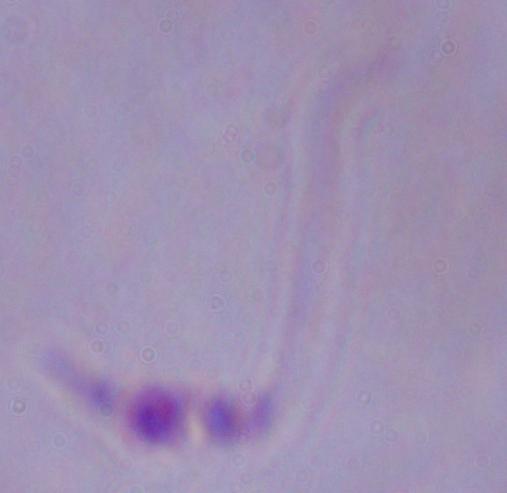
Summary:
  - Identification: Leishmania
  - Modality: photomicrograph
  - Magnification: 1000x